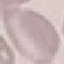
result = negative for malaria parasites
image type = cell patch, automatically extracted from a larger field of view and resized to 64 × 64 pixels
preparation = thin blood smear
capture = smartphone camera at the microscope eyepiece
stain = Giemsa